Locate and identify every blood parasite.
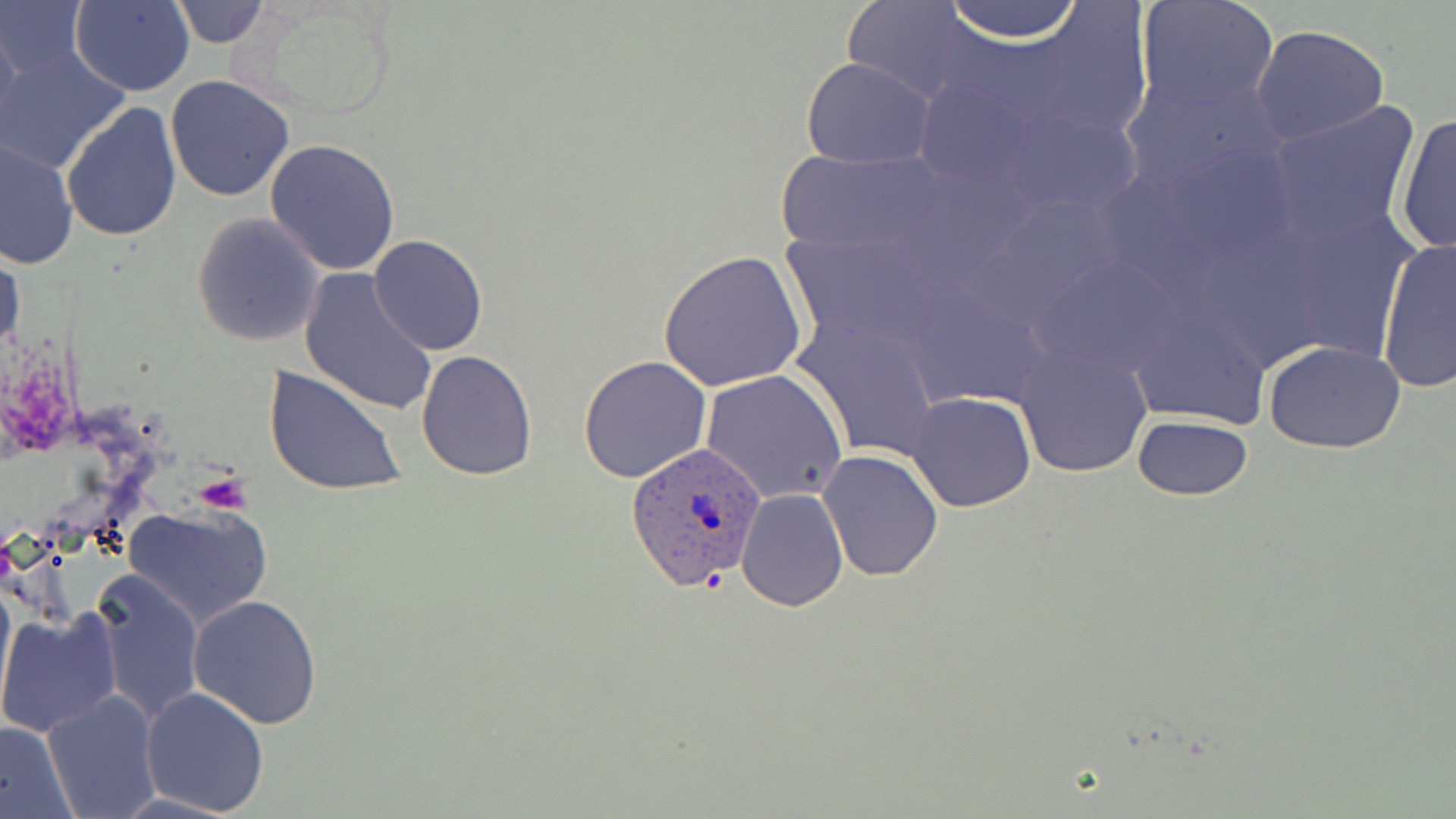

Approximate bounding boxes as [x1, y1, x2, y2] in pixels.
Plasmodium ovale-infected red blood cells: [626, 440, 769, 590].
No Plasmodium falciparum, Plasmodium malariae, Plasmodium vivax, Babesia divergens, or Trypanosoma brucei observed.

Platelet locations: [194, 470, 255, 515]. Uninfected red blood cell locations: [0, 0, 90, 83], [171, 0, 271, 48], [233, 0, 405, 122], [940, 0, 1086, 42], [1132, 0, 1282, 118], [69, 1, 196, 97], [840, 1, 992, 107], [993, 6, 1155, 149], [0, 19, 23, 145], [1249, 25, 1392, 148], [2, 47, 130, 173], [801, 56, 934, 169], [1118, 68, 1287, 199], [166, 77, 295, 203], [60, 102, 183, 241], [1262, 102, 1421, 247], [1393, 112, 1455, 256], [0, 137, 77, 271], [265, 138, 400, 275], [774, 148, 952, 260], [192, 213, 327, 347], [369, 235, 487, 355], [1376, 236, 1456, 392], [1, 243, 24, 362], [659, 251, 808, 394], [298, 267, 440, 416], [792, 312, 942, 461], [1014, 339, 1153, 479], [1263, 340, 1407, 454], [416, 348, 538, 480], [578, 356, 713, 484], [263, 366, 407, 498], [701, 369, 848, 505], [905, 391, 1036, 513], [1131, 415, 1252, 501], [817, 448, 945, 581], [736, 488, 848, 611], [120, 503, 272, 629], [89, 566, 205, 726], [0, 571, 15, 721], [187, 594, 322, 730], [0, 608, 123, 739], [140, 686, 270, 816], [41, 689, 162, 819], [0, 721, 76, 817]. Slide-level diagnosis: Plasmodium ovale. Optical microscopy. Image is 1456×819 pixels. Thin blood smear. May-Grünwald-Giemsa stain. One field of a larger specimen. Captured at 1000x magnification.